Classify this cell by malaria status.
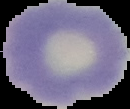
Uninfected.

From a thin blood film. Image is 130×109 pixels. Cell region segmented out of the field of view; the surrounding area is masked to black.